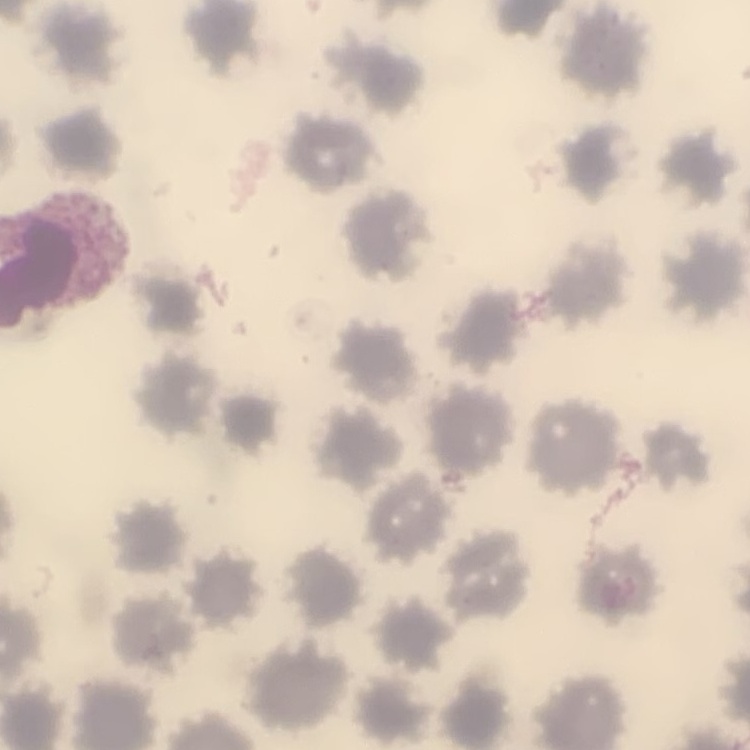

{
  "erythrocyte_morphology": "no rouleaux formation",
  "image_type": "square crop of a larger photomicrograph",
  "preparation": "thin peripheral smear",
  "stain": "Field's or Giemsa"
}